Report the malaria status of this cell.
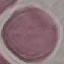

Uninfected.

Summary:
  - Stain: Giemsa
  - Capture: smartphone camera at the microscope eyepiece
  - Preparation: thin blood film
  - Image type: cell patch, automatically extracted from a larger field of view and resized to 64 × 64 pixels